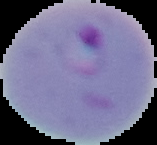

From a thin blood film. Image is 157×145 pixels. Result: Plasmodium parasites detected. The area outside the segmented cell region is set to black.